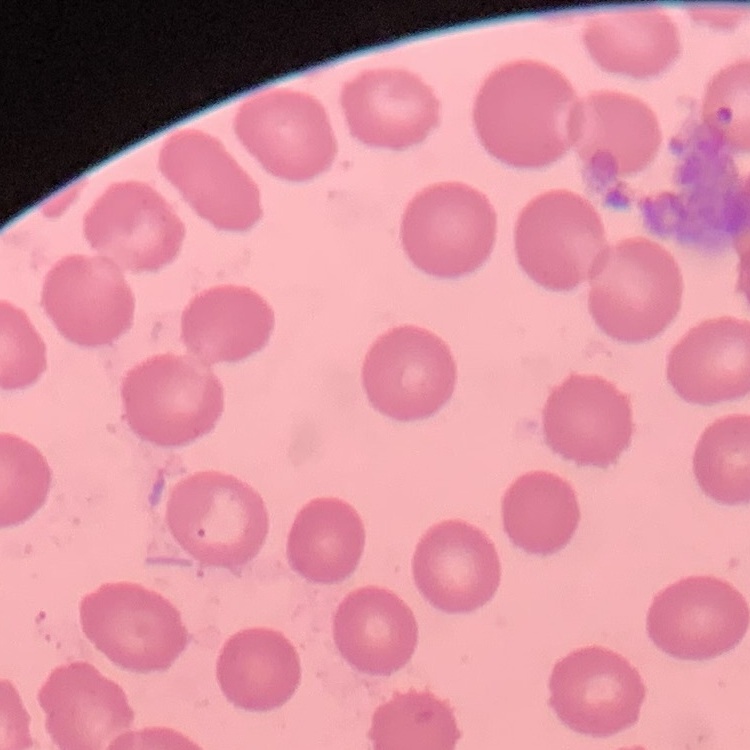

erythrocyte morphology = no rouleaux formation
stain = Field's or Giemsa
preparation = thin peripheral smear
image type = one tile cut from a larger photomicrograph